Locate every Plasmodium parasite.
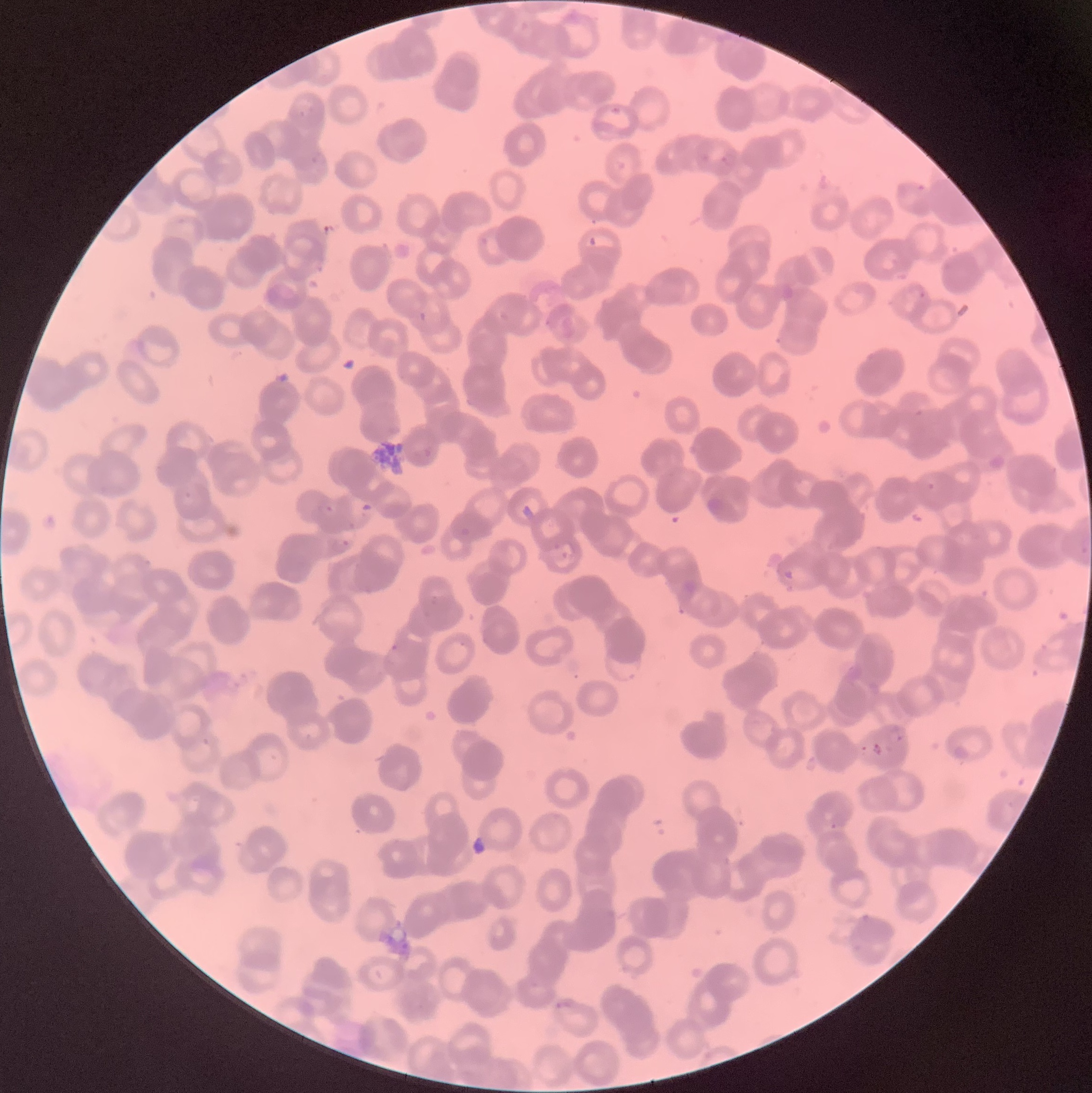

Approximate bounding boxes as [x1, y1, x2, y2] in pixels.
Plasmodium parasites: [297, 105, 317, 117], [611, 107, 623, 117], [697, 153, 710, 164], [310, 154, 320, 166], [720, 155, 729, 167], [917, 184, 926, 193], [480, 236, 489, 246], [589, 236, 598, 246], [918, 289, 926, 299], [419, 312, 428, 322], [915, 409, 924, 416], [928, 482, 935, 491], [184, 490, 192, 499], [1080, 536, 1091, 559], [342, 540, 350, 547], [555, 540, 578, 560], [783, 569, 795, 580], [390, 643, 399, 653], [610, 660, 640, 682], [889, 727, 905, 743], [873, 742, 884, 758], [829, 823, 838, 830], [552, 999, 575, 1010].
Plasmodium parasites too small for a box (approximate centers as [x, y] in pixels): [329, 508].

preparation = thin blood film
image size = 1092×1093 pixels
modality = optical microscopy
red blood cell morphology = rouleaux formation